Classify this cell by malaria status.
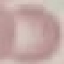
Uninfected.

Automatically extracted cell patch, resized to 64 × 64 pixels. Thin smear of blood. Giemsa-stained preparation. Photographed with a smartphone camera at the microscope eyepiece.